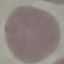
Malaria status: uninfected. Acquired by smartphone through the microscope eyepiece. Thin blood smear. Automatically extracted cell patch, resized to 64 × 64 pixels. Giemsa stain.